Describe the morphology of the red blood cells.
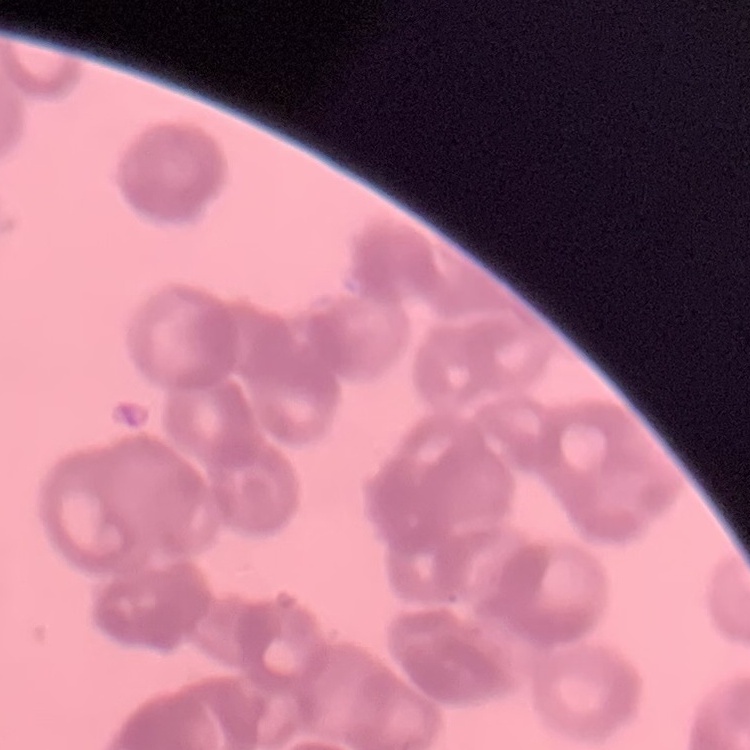
They show rouleaux formation.

Summary:
  - Image type: one tile cut from a larger photomicrograph
  - Preparation: thin blood smear
  - Stain: Field's or Giemsa